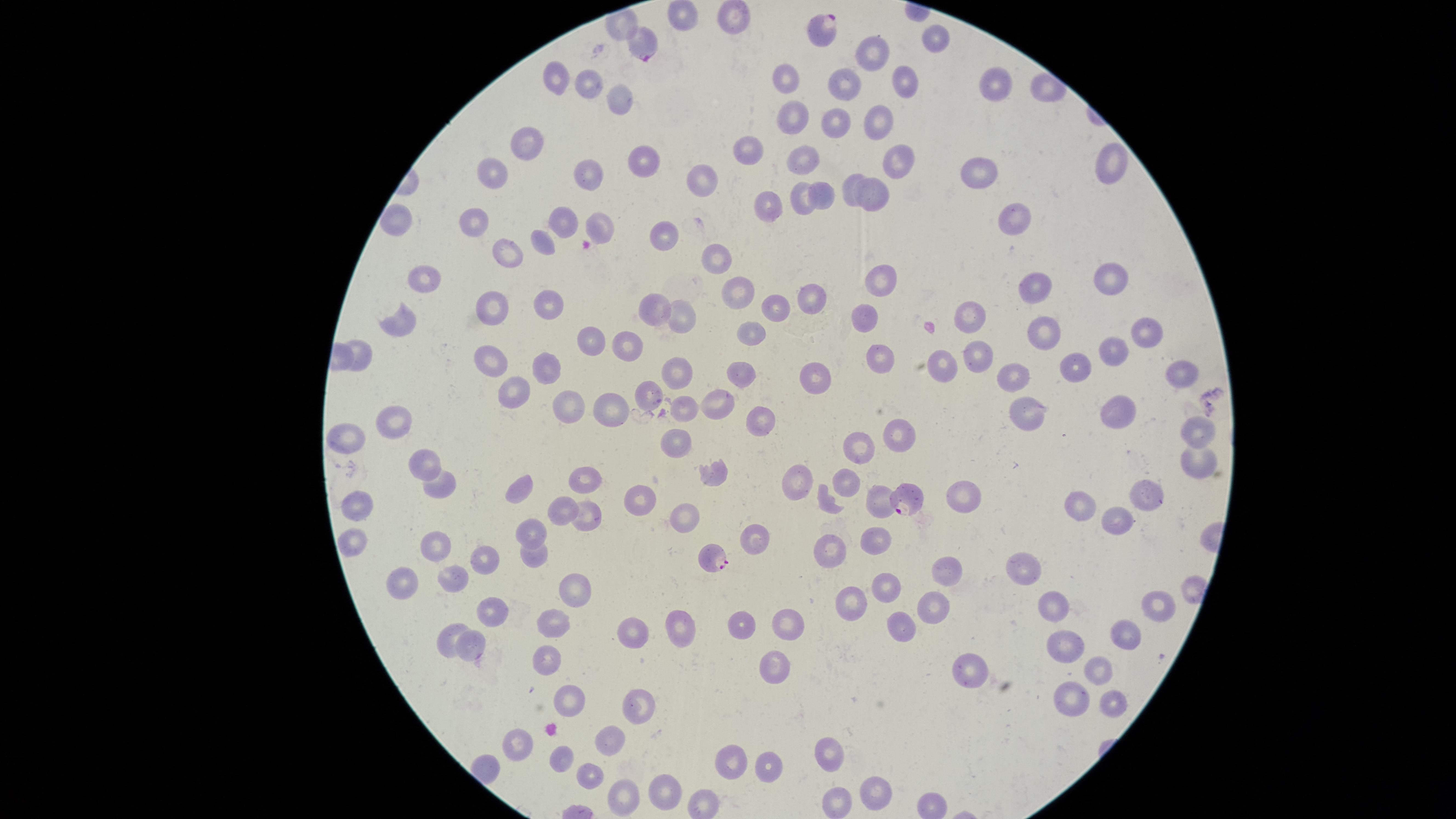

capture = smartphone photograph through the microscope eyepiece
visible region = circular
field of view = single
presence = malaria parasites identified
species = Plasmodium falciparum
image size = 1456×819 pixels
uninfected red blood cells = approximate marker points as [x, y] in pixels: [685, 9], [733, 16], [626, 21], [937, 40], [879, 52], [559, 78], [590, 80], [780, 81], [901, 81], [1001, 81], [848, 85], [621, 96], [833, 118], [786, 120], [878, 121], [520, 143], [741, 147], [643, 155], [794, 160], [896, 160], [1108, 166], [592, 167], [978, 171], [490, 179], [700, 180], [847, 190], [878, 194], [827, 196], [803, 201], [765, 204], [1016, 219], [398, 221], [561, 223], [473, 225], [599, 225], [660, 233], [548, 241], [516, 252], [718, 259], [1109, 273], [881, 278], [425, 283], [1038, 287], [736, 295], [813, 295], [548, 302], [653, 306], [493, 309], [770, 309], [865, 314], [972, 314], [681, 317], [403, 324], [1145, 331], [1040, 332], [746, 334], [591, 335], [627, 342], [362, 351], [1113, 351], [496, 355], [981, 355], [881, 357], [938, 364], [1075, 366], [1185, 366], [678, 368], [552, 369], [1015, 374], [735, 375], [823, 378], [516, 389], [642, 389], [613, 402], [715, 403], [682, 407], [566, 409], [1032, 409], [761, 417], [393, 418], [1124, 418], [1189, 427], [897, 429], [344, 436], [675, 439], [859, 445], [1196, 458], [421, 460], [715, 472], [440, 479], [580, 479], [796, 479], [841, 487], [518, 488], [957, 489], [1149, 495], [881, 498], [1081, 501], [828, 502], [640, 503], [356, 506], [566, 510], [584, 514], [1117, 516], [685, 523], [534, 537], [878, 538], [352, 541], [830, 546], [440, 548], [534, 555], [1024, 563], [486, 565], [946, 570], [450, 581], [886, 582], [405, 585], [571, 586], [1149, 600], [848, 602], [932, 603], [1053, 604], [498, 609], [792, 620], [560, 622], [682, 622], [737, 624], [901, 624], [631, 631], [1124, 631], [448, 635], [1068, 644], [476, 647], [546, 657], [778, 660], [1096, 665], [975, 671], [1070, 695], [567, 700], [1112, 700], [642, 703], [610, 740], [519, 744], [826, 748], [563, 760], [728, 761], [770, 765], [590, 772], [664, 788], [874, 791], [620, 794], [935, 800], [701, 802], [838, 804]
parasitized red blood cells = approximate marker points as [x, y] in pixels: [825, 30], [645, 45], [903, 500], [714, 557]
preparation = thin blood smear
stain = Giemsa